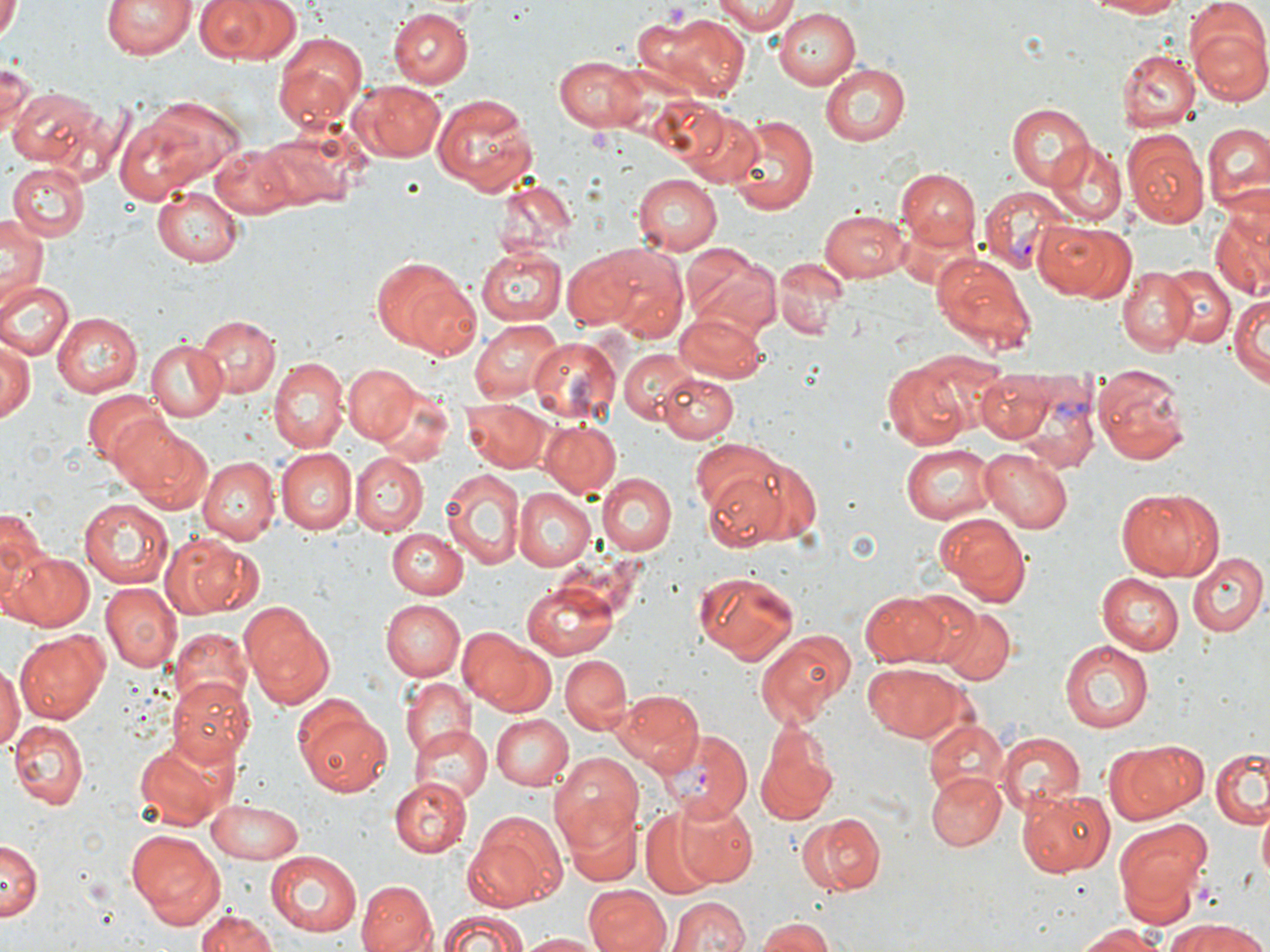
slide-level diagnosis = Plasmodium vivax
image size = 1270×952 pixels
Plasmodium vivax-infected red blood cell locations = approximate bounding boxes as (x1,y1)-(x2,y2) corner pairs in pixels: (978,185)-(1071,271), (1020,363)-(1103,479), (662,728)-(751,821)
magnification = 1000x
uninfected red blood cell locations = approximate bounding boxes as (x1,y1)-(x2,y2) corner pairs in pixels: (100,0)-(193,61), (192,0)-(297,64), (711,0)-(804,33), (1083,0)-(1191,18), (1,4)-(20,39), (388,6)-(474,89), (773,7)-(861,88), (636,11)-(751,104), (1188,18)-(1270,107), (271,31)-(368,131), (1119,49)-(1200,132), (551,54)-(647,132), (0,58)-(38,142), (819,62)-(910,146), (349,80)-(446,163), (7,84)-(109,174), (432,90)-(539,194), (133,94)-(246,187), (1006,101)-(1092,190), (677,109)-(765,190), (115,111)-(208,202), (728,113)-(818,214), (1203,122)-(1270,213), (258,127)-(359,211), (1122,129)-(1209,230), (1043,139)-(1128,226), (210,141)-(300,219), (9,163)-(89,241), (898,170)-(981,254), (630,173)-(721,254), (491,178)-(578,260), (152,188)-(243,268), (820,207)-(911,280), (1212,211)-(1269,300), (0,214)-(48,300), (1035,220)-(1132,302), (477,245)-(566,326), (596,246)-(689,342), (561,250)-(638,327), (929,250)-(1038,360), (684,252)-(784,339), (369,255)-(481,360), (772,258)-(847,341), (1117,264)-(1196,355), (1165,267)-(1233,348), (0,279)-(74,359), (1232,293)-(1269,386), (51,312)-(141,398), (675,312)-(768,382), (194,313)-(279,398), (470,318)-(563,402), (527,335)-(621,423), (0,339)-(35,425), (143,340)-(227,421), (618,346)-(698,423), (267,357)-(348,454), (882,363)-(967,450), (342,364)-(419,444), (1092,365)-(1193,464), (658,370)-(737,441), (974,372)-(1056,440), (369,377)-(457,464), (81,389)-(167,468), (464,400)-(548,471), (105,413)-(207,507), (538,420)-(623,497), (689,444)-(800,548), (901,444)-(997,524), (980,448)-(1072,532), (277,450)-(357,534), (350,453)-(427,535), (741,455)-(824,545), (199,457)-(279,544), (439,468)-(527,570), (601,472)-(677,555), (510,488)-(594,572), (1113,488)-(1224,582), (80,497)-(174,587), (0,508)-(47,616), (934,513)-(1031,606), (388,529)-(463,598), (169,537)-(260,616), (5,549)-(93,632), (1186,551)-(1266,636), (690,571)-(797,664), (1096,572)-(1185,655), (100,582)-(178,673), (520,582)-(620,659), (902,589)-(986,669), (860,590)-(953,665), (380,599)-(464,681), (239,601)-(337,710), (937,606)-(1015,685), (12,628)-(115,723), (169,629)-(253,719), (755,629)-(853,726), (461,632)-(556,716), (1059,640)-(1155,734), (559,654)-(633,734), (861,662)-(970,743), (0,666)-(20,756), (399,676)-(473,756), (167,677)-(255,767), (614,689)-(704,774), (298,706)-(394,796), (490,713)-(573,791), (9,720)-(87,809), (926,723)-(1006,806), (408,724)-(492,805), (756,728)-(836,826), (996,732)-(1084,814), (134,735)-(240,831), (1108,738)-(1209,825), (1211,747)-(1270,830), (548,753)-(644,853), (927,773)-(1006,852), (393,777)-(472,858), (1018,788)-(1115,878), (677,800)-(758,888), (207,801)-(305,862), (560,804)-(643,886), (641,808)-(721,896), (1257,810)-(1270,878), (462,813)-(567,911), (798,814)-(885,897), (1113,819)-(1213,916), (125,828)-(227,930), (0,839)-(40,922), (265,850)-(360,935), (357,880)-(437,952), (583,886)-(671,952), (671,897)-(750,952), (194,909)-(280,951), (432,909)-(532,952), (754,916)-(838,952), (1162,919)-(1263,952), (1071,921)-(1174,951), (517,932)-(603,951)
stain = May-Grünwald-Giemsa
field of view = one of a larger specimen
modality = optical microscopy
preparation = thin blood smear
platelet locations = approximate bounding boxes as (x1,y1)-(x2,y2) corner pairs in pixels: (665,4)-(692,33), (586,124)-(615,151)